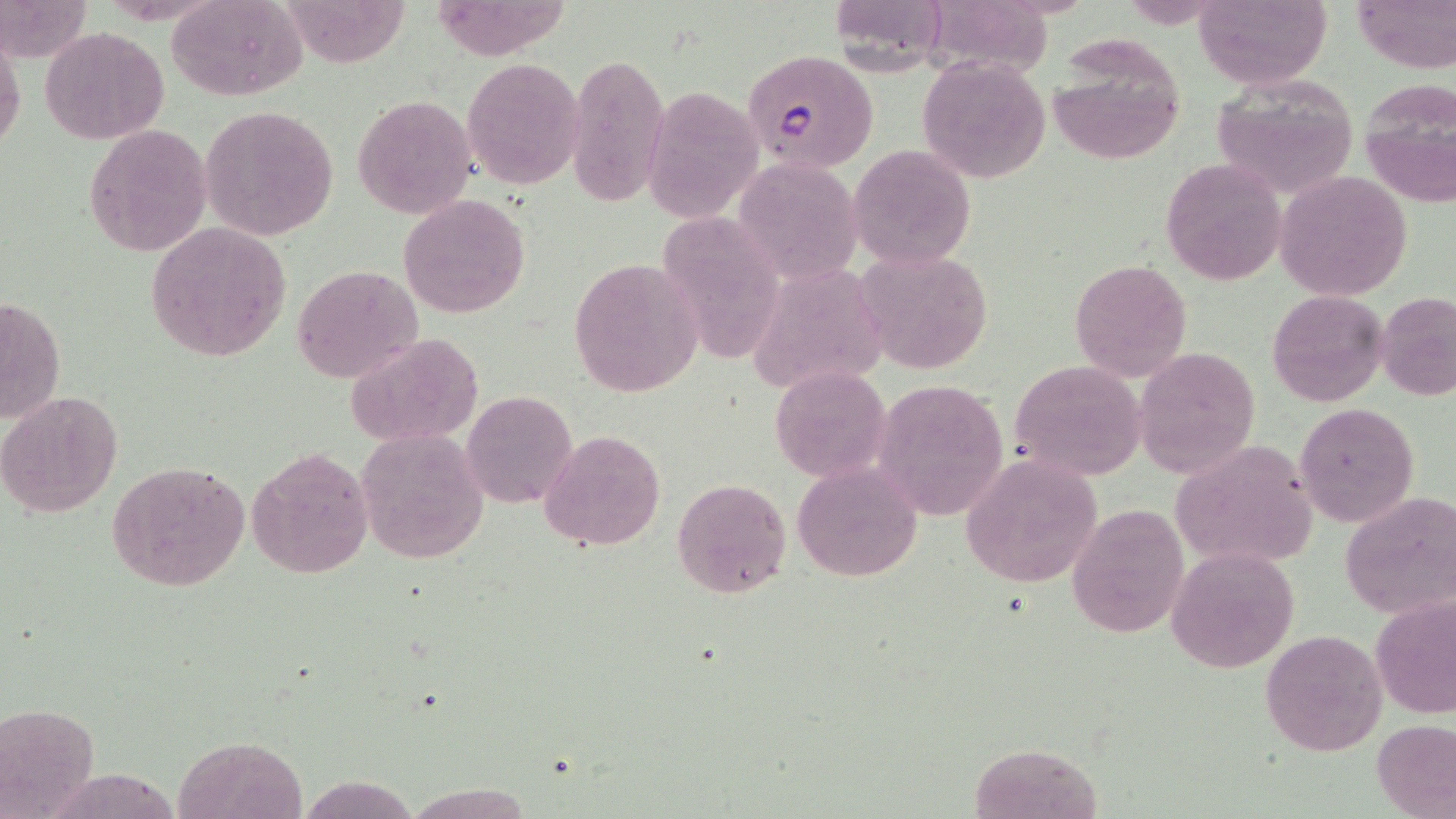
plasmodium_falciparum_infected_red_blood_cell_locations: 'approximate bounding boxes as named x1/y1/x2/y2 corners in pixels: (x1=741, y1=49, x2=879, y2=174)'
slide_level_diagnosis: Plasmodium falciparum
preparation: thin blood film
field_of_view: single
magnification: 1000x
uninfected_red_blood_cell_locations: 'approximate bounding boxes as named x1/y1/x2/y2 corners in pixels: (x1=0, y1=0, x2=92, y2=65), (x1=168, y1=0, x2=307, y2=101), (x1=290, y1=0, x2=412, y2=67), (x1=828, y1=0, x2=950, y2=69), (x1=921, y1=0, x2=1058, y2=88), (x1=1193, y1=0, x2=1333, y2=91), (x1=1353, y1=0, x2=1455, y2=73), (x1=429, y1=1, x2=573, y2=61), (x1=0, y1=27, x2=25, y2=163), (x1=40, y1=27, x2=169, y2=144), (x1=1047, y1=36, x2=1186, y2=165), (x1=564, y1=49, x2=669, y2=209), (x1=461, y1=57, x2=585, y2=189), (x1=918, y1=57, x2=1051, y2=183), (x1=1211, y1=74, x2=1360, y2=199), (x1=1359, y1=80, x2=1455, y2=212), (x1=643, y1=86, x2=762, y2=223), (x1=351, y1=95, x2=477, y2=218), (x1=199, y1=104, x2=338, y2=242), (x1=83, y1=124, x2=212, y2=256), (x1=848, y1=143, x2=976, y2=270), (x1=741, y1=154, x2=863, y2=281), (x1=1161, y1=157, x2=1288, y2=286), (x1=1275, y1=171, x2=1411, y2=302), (x1=398, y1=194, x2=531, y2=318), (x1=661, y1=205, x2=783, y2=359), (x1=145, y1=221, x2=292, y2=363), (x1=853, y1=249, x2=995, y2=374), (x1=751, y1=255, x2=882, y2=390), (x1=568, y1=256, x2=703, y2=396), (x1=1069, y1=258, x2=1193, y2=383), (x1=293, y1=264, x2=423, y2=382), (x1=1267, y1=290, x2=1390, y2=409), (x1=1377, y1=291, x2=1456, y2=401), (x1=0, y1=293, x2=65, y2=430), (x1=343, y1=333, x2=481, y2=447), (x1=1133, y1=347, x2=1260, y2=477), (x1=1009, y1=360, x2=1147, y2=481), (x1=768, y1=365, x2=888, y2=481), (x1=870, y1=379, x2=1008, y2=522), (x1=0, y1=389, x2=123, y2=518), (x1=462, y1=391, x2=577, y2=508), (x1=1294, y1=401, x2=1418, y2=530), (x1=356, y1=427, x2=488, y2=564), (x1=541, y1=428, x2=665, y2=551), (x1=1173, y1=441, x2=1322, y2=568), (x1=248, y1=446, x2=375, y2=580), (x1=960, y1=454, x2=1104, y2=590), (x1=107, y1=460, x2=249, y2=590), (x1=794, y1=464, x2=922, y2=581), (x1=671, y1=476, x2=792, y2=599), (x1=1340, y1=490, x2=1456, y2=620), (x1=1066, y1=505, x2=1189, y2=639), (x1=1167, y1=545, x2=1300, y2=675), (x1=1371, y1=593, x2=1455, y2=719), (x1=1260, y1=628, x2=1387, y2=758), (x1=0, y1=701, x2=101, y2=817), (x1=1372, y1=718, x2=1455, y2=817), (x1=175, y1=736, x2=307, y2=819), (x1=962, y1=742, x2=1105, y2=819), (x1=62, y1=765, x2=192, y2=819), (x1=296, y1=774, x2=415, y2=817), (x1=406, y1=781, x2=528, y2=818)'
image_size: 1456×819 pixels
modality: light microscopy
stain: May-Grünwald-Giemsa